Identify the parasite.
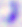

This is Toxoplasma gondii.

magnification: 400x
modality: photomicrograph